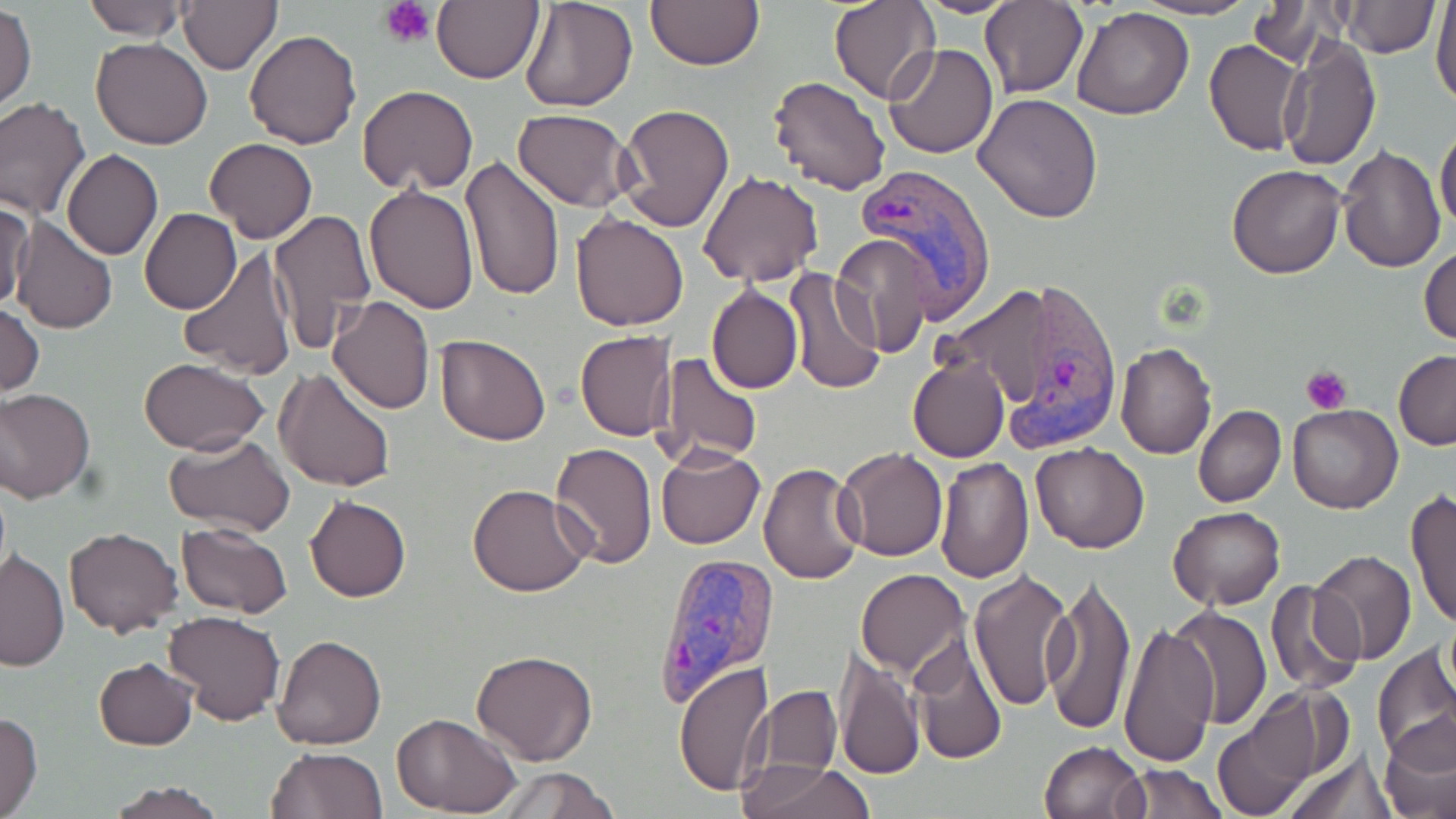

{
  "slide_level_diagnosis": "Plasmodium vivax",
  "platelet_locations": "approximate bounding boxes as (x1,y1)-(x2,y2) corner pairs in pixels: (379,0)-(437,46), (1301,364)-(1354,413)",
  "stain": "May-Grünwald-Giemsa",
  "plasmodium_vivax_infected_red_blood_cell_locations": "approximate bounding boxes as (x1,y1)-(x2,y2) corner pairs in pixels: (856,165)-(997,319), (994,278)-(1125,447), (656,551)-(777,706)",
  "field_of_view": "one of a larger specimen",
  "preparation": "thin blood smear",
  "modality": "optical microscopy",
  "image_size": "1456×819 pixels",
  "magnification": "1000x",
  "uninfected_red_blood_cell_locations": "approximate bounding boxes as (x1,y1)-(x2,y2) corner pairs in pixels: (80,0)-(193,40), (177,0)-(282,75), (431,0)-(542,85), (517,0)-(637,113), (646,0)-(763,70), (830,0)-(939,103), (910,0)-(1022,16), (1131,0)-(1260,21), (1430,0)-(1456,109), (979,1)-(1087,99), (1340,1)-(1437,57), (1249,2)-(1343,67), (1,5)-(36,109), (1072,6)-(1195,121), (243,29)-(362,149), (91,38)-(214,150), (1203,38)-(1305,157), (1278,38)-(1381,171), (884,44)-(998,159), (767,74)-(893,196), (357,85)-(479,195), (974,93)-(1103,223), (0,98)-(91,220), (615,103)-(736,232), (513,109)-(633,211), (1435,126)-(1456,230), (206,137)-(317,244), (1338,143)-(1445,272), (62,150)-(163,259), (460,156)-(566,303), (1228,164)-(1345,278), (698,170)-(823,289), (364,184)-(479,314), (2,199)-(34,310), (139,208)-(241,314), (268,209)-(376,354), (569,212)-(689,331), (11,216)-(119,334), (830,236)-(929,360), (1420,247)-(1456,345), (178,248)-(298,380), (783,269)-(885,396), (706,284)-(802,396), (327,295)-(435,415), (0,298)-(43,399), (575,331)-(676,441), (434,333)-(552,447), (1116,342)-(1218,459), (1393,350)-(1456,449), (654,352)-(762,466), (908,355)-(1010,463), (140,357)-(269,454), (275,368)-(397,495), (0,388)-(96,503), (1193,404)-(1286,508), (1287,405)-(1402,513), (164,435)-(296,538), (1029,442)-(1149,552), (549,444)-(659,569), (656,445)-(765,550), (835,447)-(947,562), (933,457)-(1035,583), (757,464)-(866,585), (468,484)-(591,598), (1406,490)-(1456,630), (306,496)-(411,603), (1170,506)-(1285,611), (176,522)-(295,618), (65,527)-(183,638), (1310,548)-(1418,666), (0,549)-(70,671), (967,567)-(1075,710), (856,569)-(970,679), (1042,573)-(1137,736), (1264,579)-(1366,698), (1165,606)-(1270,729), (164,609)-(285,724), (1118,619)-(1220,767), (907,631)-(1009,765), (273,635)-(387,750), (1373,644)-(1456,762), (471,649)-(598,767), (833,650)-(924,781), (94,658)-(198,750), (674,660)-(773,796), (760,685)-(841,778), (1213,696)-(1328,815), (0,710)-(42,819), (393,713)-(521,818), (1381,719)-(1456,819), (1039,740)-(1148,819), (1285,747)-(1395,819), (264,749)-(387,818), (732,759)-(877,819), (1115,762)-(1226,819), (487,766)-(621,819), (102,780)-(229,819)"
}